Assess for malaria.
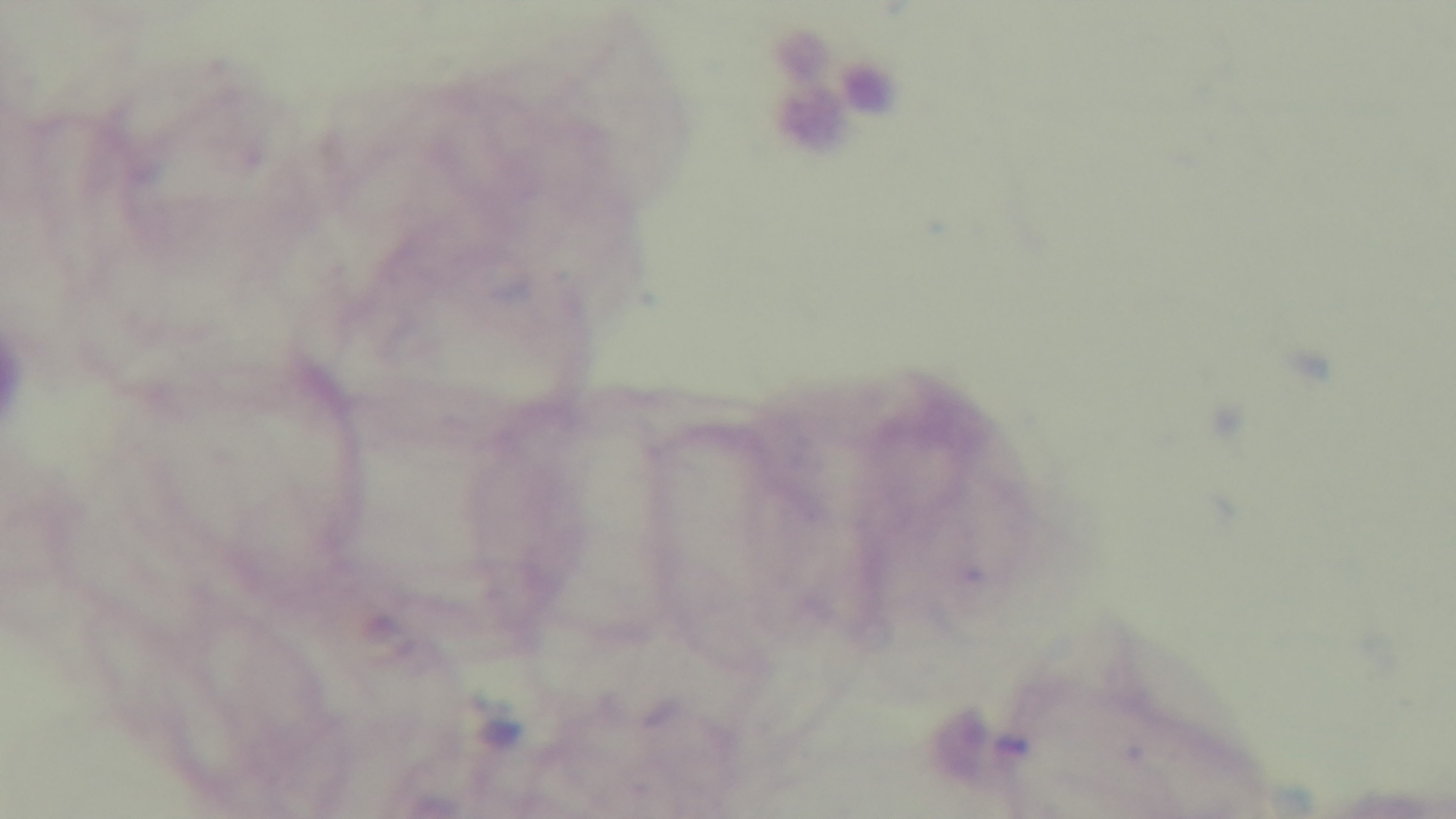
It is uninfected.

Summary:
  - Capture: mounted 4K digital camera
  - Objective: 100x oil immersion
  - Stain: Giemsa
  - Field of view: single
  - Preparation: thick
  - Modality: light microscopy